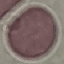

Summary:
  - Malaria status: uninfected
  - Preparation: thin blood film
  - Image type: automatically extracted cell patch, resized to 64 × 64 pixels
  - Capture: smartphone through the microscope eyepiece
  - Stain: Giemsa